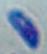

Summary:
  - Modality: photomicrograph
  - Magnification: 1000x
  - Identification: Toxoplasma gondii